Assess this cell for malaria.
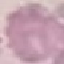
Uninfected.

Summary:
  - Preparation: thin blood smear
  - Stain: Giemsa
  - Image type: cell patch, automatically extracted from a larger field of view and resized to 64 × 64 pixels
  - Capture: smartphone through the microscope eyepiece